Assess this cell for malaria.
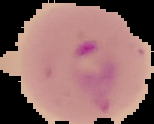
Parasitized.

Cell region segmented out of the field of view; the surrounding area is masked to black. From a thin blood smear. Image is 154×124 pixels.